Classify this cell by malaria status.
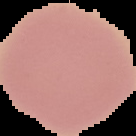

It is uninfected.

preparation = thin blood film
image type = segmented cell region with the area outside set to black
image size = 136×136 pixels